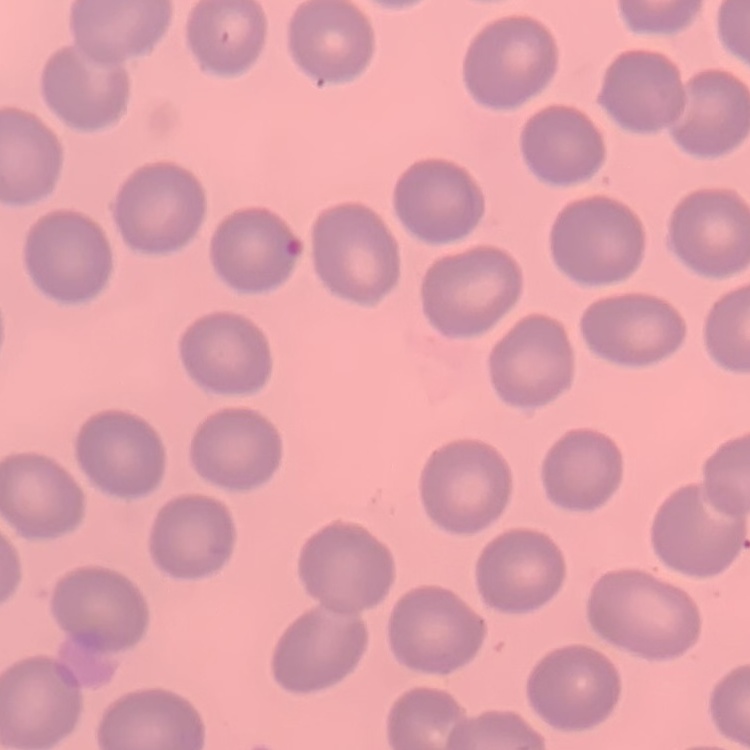
The red blood cells show no rouleaux formation. One tile cut from a larger photomicrograph. Stained with either Field's or Giemsa. Thin blood film.